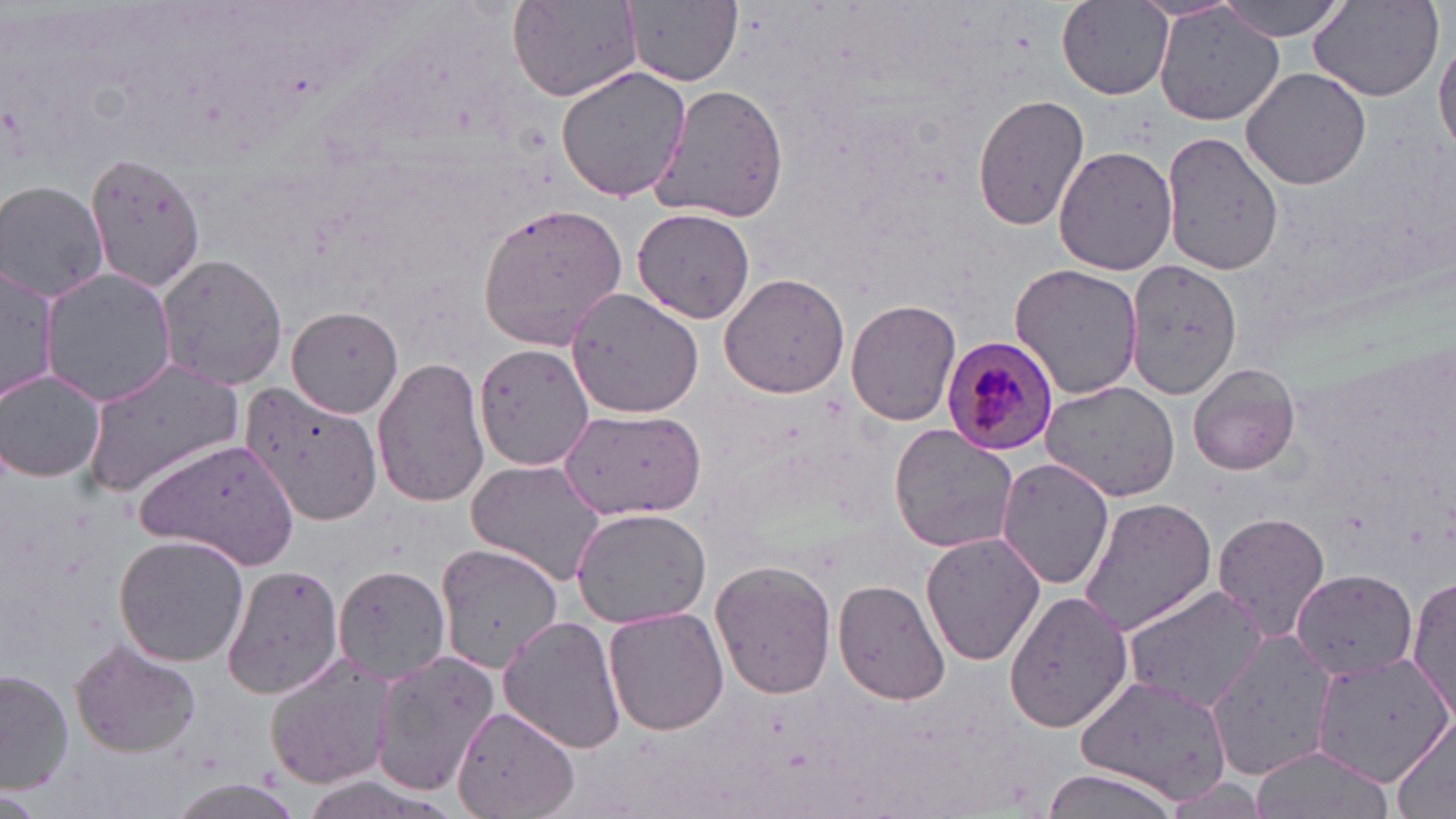

Approximate bounding boxes as (x1, y1, x2, y2) in pixels. Plasmodium malariae-infected red blood cell locations: (942, 335, 1061, 456). Uninfected red blood cell locations: (508, 0, 643, 101), (1217, 0, 1350, 40), (1308, 0, 1444, 102), (625, 2, 742, 86), (1058, 2, 1174, 98), (1153, 5, 1286, 128), (1434, 36, 1456, 154), (555, 64, 692, 203), (1239, 66, 1371, 190), (647, 80, 792, 224), (972, 94, 1090, 231), (1162, 131, 1285, 276), (1054, 145, 1178, 275), (85, 153, 211, 291), (0, 180, 110, 305), (476, 199, 630, 350), (633, 208, 756, 325), (154, 252, 289, 391), (1123, 259, 1241, 397), (1008, 263, 1144, 401), (0, 265, 59, 403), (41, 269, 176, 409), (718, 273, 850, 398), (563, 286, 707, 419), (847, 297, 961, 426), (286, 304, 404, 419), (474, 342, 593, 471), (372, 355, 490, 509), (81, 359, 246, 495), (1188, 362, 1301, 475), (1, 371, 106, 483), (1039, 379, 1180, 502), (240, 382, 382, 527), (557, 407, 707, 520), (888, 426, 1021, 553), (137, 438, 298, 570), (995, 456, 1116, 590), (465, 458, 610, 587), (1079, 498, 1217, 634), (572, 507, 711, 626), (1212, 511, 1332, 643), (921, 531, 1045, 667), (114, 533, 251, 667), (434, 543, 561, 674), (710, 560, 837, 700), (222, 563, 345, 700), (333, 564, 449, 683), (1292, 569, 1415, 679), (1407, 575, 1455, 720), (834, 578, 951, 705), (1123, 584, 1269, 714), (1002, 589, 1133, 733), (603, 607, 730, 736), (499, 613, 627, 755), (1205, 634, 1339, 779), (70, 639, 204, 757), (368, 650, 499, 795), (263, 652, 404, 790), (1308, 655, 1451, 787), (0, 667, 72, 795), (1074, 672, 1231, 801), (450, 705, 578, 819), (1386, 716, 1455, 819), (1252, 746, 1386, 819), (1035, 769, 1183, 819), (162, 777, 308, 819). Slide-level diagnosis: Plasmodium malariae. 1000x magnification. Optical microscopy. May-Grünwald-Giemsa stain. Thin blood film. Single field of view. Image is 1456×819 pixels.